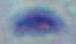

{
  "modality": "micrograph",
  "identification": "Toxoplasma gondii",
  "magnification": "1000x"
}